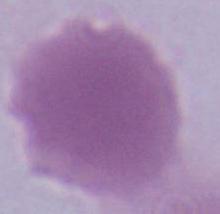
An erythrocyte is seen. Micrograph. 1000x magnification.